State which cell type is depicted.
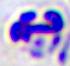
This is a leukocyte.

{
  "magnification": "400x",
  "modality": "micrograph"
}